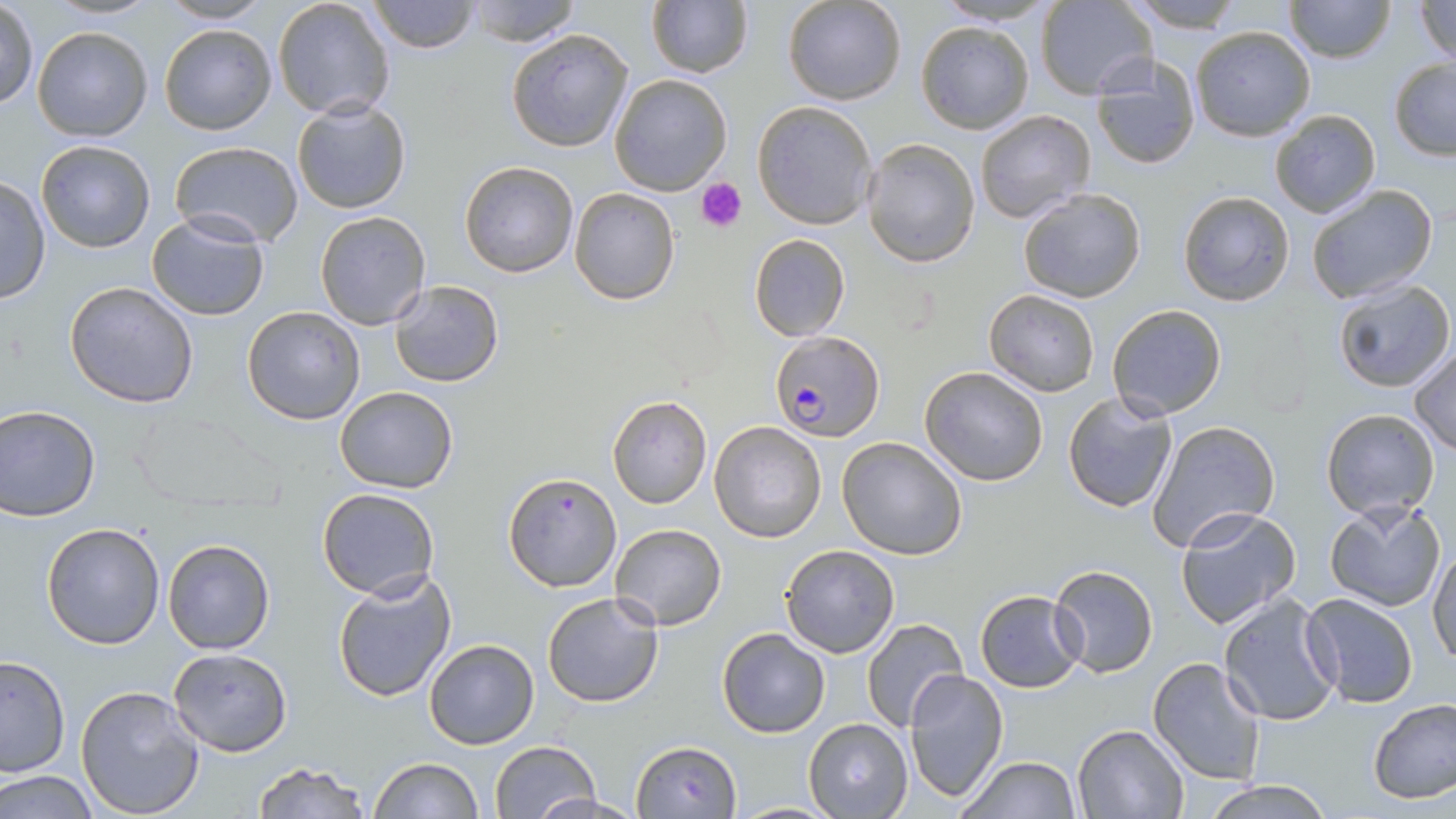

Approximate bounding boxes as (x1,y1)-(x2,y2) corner pairs in pixels. Plasmodium falciparum-infected red blood cell locations: (770,329)-(883,439). Platelet locations: (696,177)-(748,231). Uninfected red blood cell locations: (272,0)-(395,121), (369,0)-(479,54), (462,0)-(582,46), (783,0)-(907,105), (934,0)-(1058,27), (1122,0)-(1249,32), (1284,0)-(1395,64), (1408,0)-(1456,63), (160,1)-(270,25), (646,1)-(752,78), (1039,1)-(1157,100), (1,3)-(38,109), (916,20)-(1034,135), (158,23)-(277,135), (32,25)-(152,141), (1190,25)-(1316,140), (506,28)-(635,152), (1088,52)-(1201,171), (1388,58)-(1456,159), (610,73)-(732,195), (292,97)-(411,214), (751,100)-(877,230), (974,110)-(1096,224), (1269,110)-(1380,218), (862,137)-(979,267), (36,139)-(156,254), (169,141)-(303,246), (459,161)-(578,278), (0,175)-(50,306), (1305,183)-(1438,303), (569,187)-(681,306), (1016,187)-(1147,302), (1177,190)-(1294,306), (315,210)-(430,329), (147,212)-(271,320), (749,232)-(850,341), (1331,279)-(1455,394), (389,280)-(504,386), (64,281)-(200,408), (983,290)-(1101,397), (1106,303)-(1227,421), (241,306)-(366,424), (1409,348)-(1456,455), (919,366)-(1049,486), (333,386)-(458,494), (1062,392)-(1178,513), (606,394)-(714,510), (0,403)-(101,522), (131,406)-(277,514), (1319,407)-(1440,517), (1148,420)-(1280,550), (709,421)-(828,542), (837,435)-(968,558), (502,470)-(623,592), (316,488)-(438,602), (1325,498)-(1447,614), (1174,505)-(1301,629), (41,522)-(165,649), (609,524)-(727,629), (163,537)-(276,655), (780,544)-(899,658), (1428,544)-(1455,669), (1050,564)-(1157,677), (332,572)-(455,704), (974,590)-(1087,691), (542,591)-(665,708), (1217,592)-(1344,726), (1301,595)-(1417,708), (861,617)-(969,734), (717,628)-(830,738), (425,638)-(539,749), (169,648)-(292,755), (0,656)-(71,777), (1148,658)-(1266,787), (903,669)-(1008,801), (75,683)-(205,818), (1368,697)-(1456,804), (805,717)-(914,818), (1074,723)-(1189,818), (489,740)-(603,819), (630,740)-(743,817), (956,755)-(1081,818), (369,757)-(484,819), (252,762)-(371,819), (1,771)-(100,817), (1197,777)-(1331,817), (529,792)-(650,818), (729,801)-(843,817). Slide-level diagnosis: Plasmodium falciparum. Single field of view. 1000x magnification. Light microscopy. Thin blood smear. Image is 1456×819 pixels. May-Grünwald-Giemsa stain.